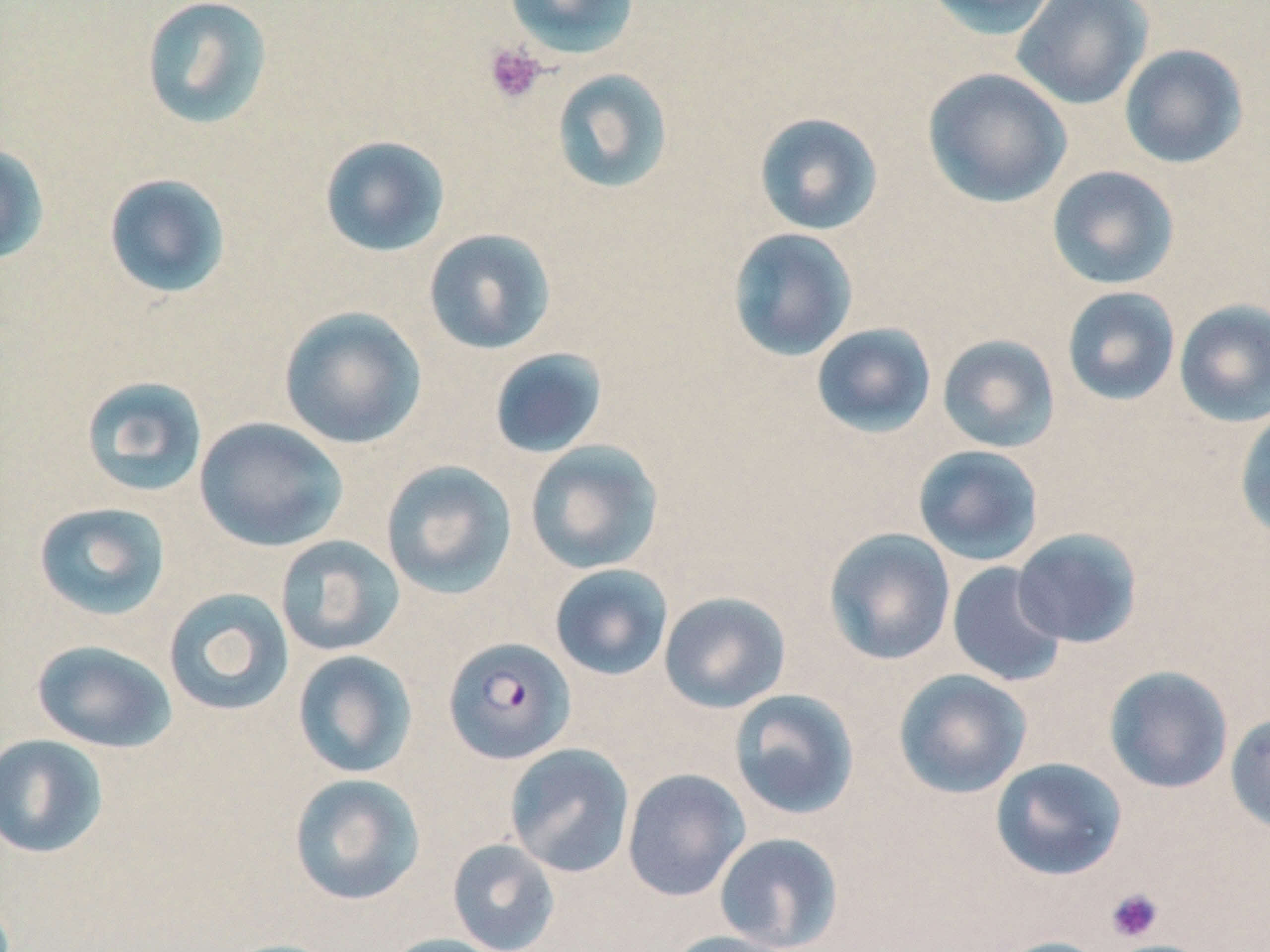
Approximate bounding boxes as (x1, y1, x2, y2) in pixels. Platelet locations: (484, 42, 547, 105), (1106, 887, 1164, 942). Uninfected red blood cell locations: (503, 0, 640, 60), (922, 0, 1061, 39), (140, 1, 274, 131), (1012, 1, 1154, 109), (1119, 44, 1248, 169), (551, 68, 674, 194), (921, 68, 1072, 208), (753, 112, 884, 236), (319, 135, 451, 257), (0, 144, 50, 267), (1046, 165, 1180, 290), (103, 173, 232, 300), (727, 227, 858, 361), (423, 228, 557, 355), (1061, 286, 1181, 407), (1173, 299, 1270, 427), (278, 306, 428, 450), (811, 322, 937, 438), (936, 334, 1061, 453), (489, 348, 608, 459), (80, 375, 209, 498), (1234, 406, 1270, 543), (194, 417, 348, 552), (525, 439, 664, 575), (912, 444, 1044, 566), (380, 460, 518, 599), (31, 501, 171, 621), (823, 528, 956, 666), (1011, 528, 1143, 648), (274, 535, 405, 657), (946, 562, 1067, 688), (549, 564, 674, 681), (163, 587, 295, 716), (658, 591, 792, 714), (30, 639, 178, 753), (292, 650, 418, 779), (1103, 665, 1234, 794), (893, 669, 1032, 799), (728, 688, 860, 820), (1225, 712, 1270, 836), (0, 733, 109, 859), (504, 743, 635, 878), (989, 757, 1128, 881), (621, 768, 750, 902), (288, 772, 426, 906), (714, 832, 844, 951), (447, 838, 561, 951), (662, 930, 795, 952), (380, 934, 511, 952), (990, 936, 1112, 952), (215, 938, 345, 952). Plasmodium falciparum-infected red blood cell locations: (442, 636, 576, 765). Slide-level diagnosis: Plasmodium falciparum. Light microscopy. Captured at 1000x magnification. Image is 1270×952 pixels. One field of a larger specimen. May-Grünwald-Giemsa stain. Thin blood film.